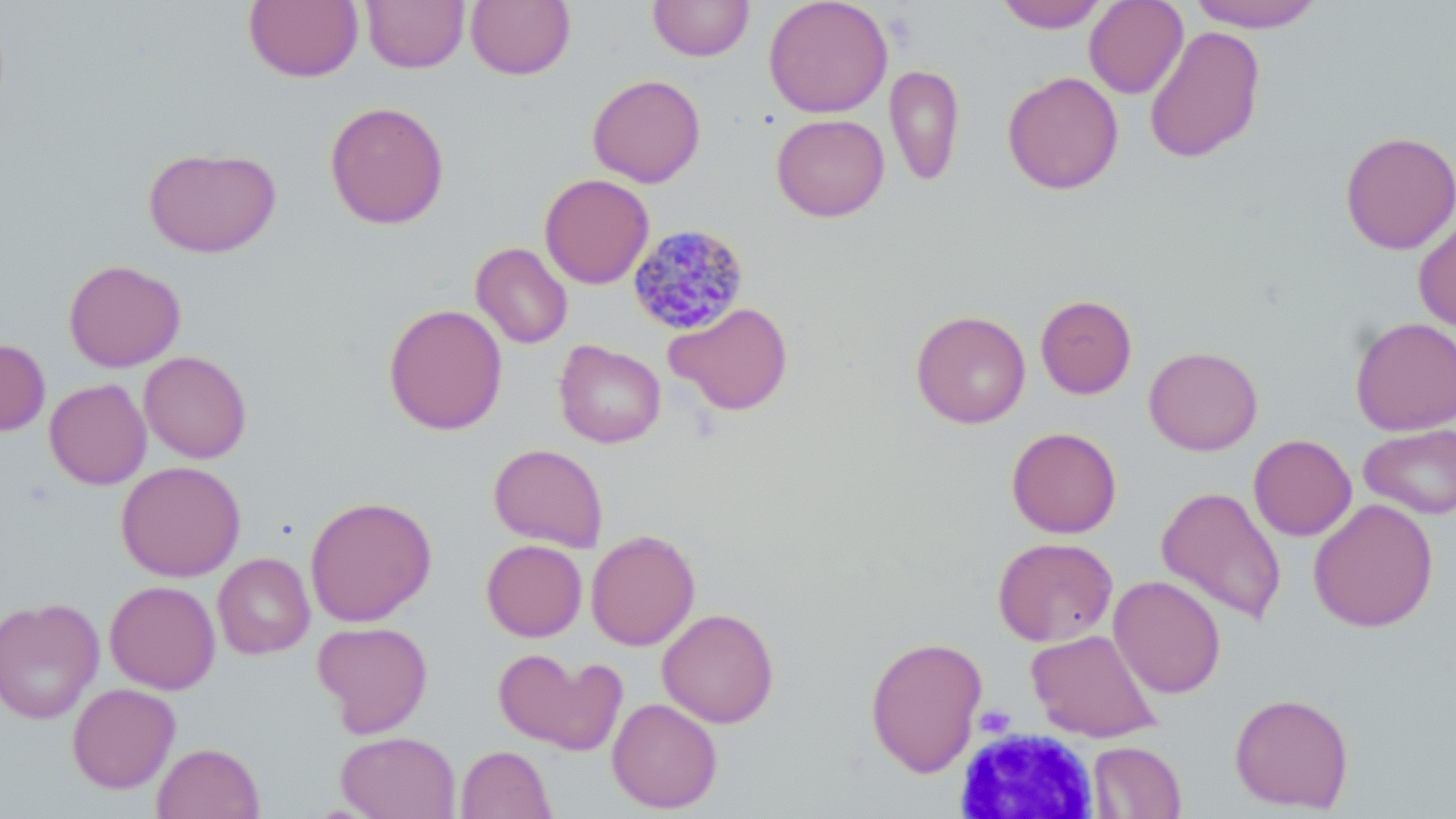

Approximate bounding boxes as [x1, y1, x2, y2] in pixels. White blood cell locations: [954, 728, 1101, 818]. Uninfected red blood cell locations: [361, 0, 469, 72], [466, 0, 576, 80], [648, 0, 754, 61], [764, 0, 893, 118], [994, 0, 1110, 32], [1084, 0, 1188, 98], [244, 1, 363, 82], [1186, 1, 1325, 32], [1144, 25, 1266, 164], [884, 64, 964, 187], [1002, 70, 1124, 195], [587, 74, 706, 188], [324, 100, 450, 230], [771, 113, 889, 221], [1339, 131, 1456, 254], [143, 147, 282, 257], [539, 174, 654, 289], [1414, 215, 1456, 332], [471, 242, 573, 349], [63, 259, 186, 372], [1035, 294, 1137, 399], [665, 302, 794, 415], [383, 303, 508, 434], [911, 310, 1031, 429], [1350, 316, 1456, 435], [0, 338, 50, 436], [554, 340, 666, 448], [1143, 346, 1263, 455], [139, 351, 252, 463], [44, 379, 152, 489], [1358, 423, 1456, 519], [1006, 426, 1122, 538], [1248, 434, 1357, 541], [488, 443, 608, 552], [116, 460, 246, 581], [1156, 485, 1287, 626], [305, 495, 437, 626], [1308, 498, 1439, 632], [586, 529, 700, 651], [992, 537, 1118, 646], [481, 539, 588, 642], [213, 553, 315, 659], [1109, 575, 1227, 698], [104, 580, 221, 694], [0, 592, 220, 707], [0, 597, 104, 725], [657, 608, 780, 728], [312, 620, 433, 737], [1026, 629, 1162, 742], [864, 635, 987, 777], [493, 648, 625, 756], [67, 683, 180, 793], [1229, 692, 1355, 813], [607, 697, 723, 814], [336, 731, 460, 819], [1088, 741, 1187, 818], [152, 742, 264, 819], [456, 745, 556, 819]. Plasmodium malariae-infected red blood cell locations: [626, 223, 749, 335]. Slide-level diagnosis: Plasmodium malariae. Image is 1456×819 pixels. One field of a larger specimen. Optical microscopy. 1000x magnification. Thin blood smear. May-Grünwald-Giemsa stain.